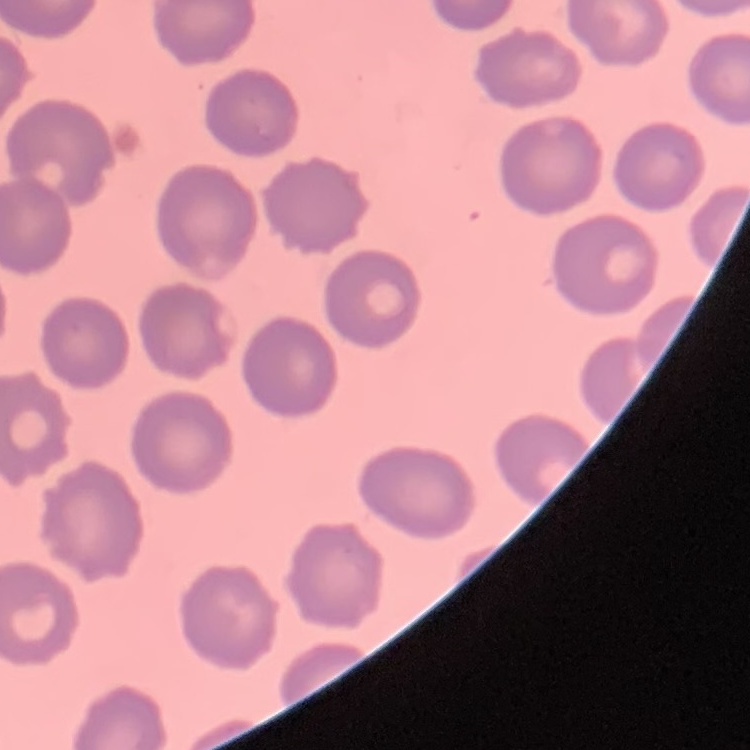 The erythrocytes show no rouleaux formation. Field's or Giemsa stain. Square crop of a larger photomicrograph. Thin blood film.